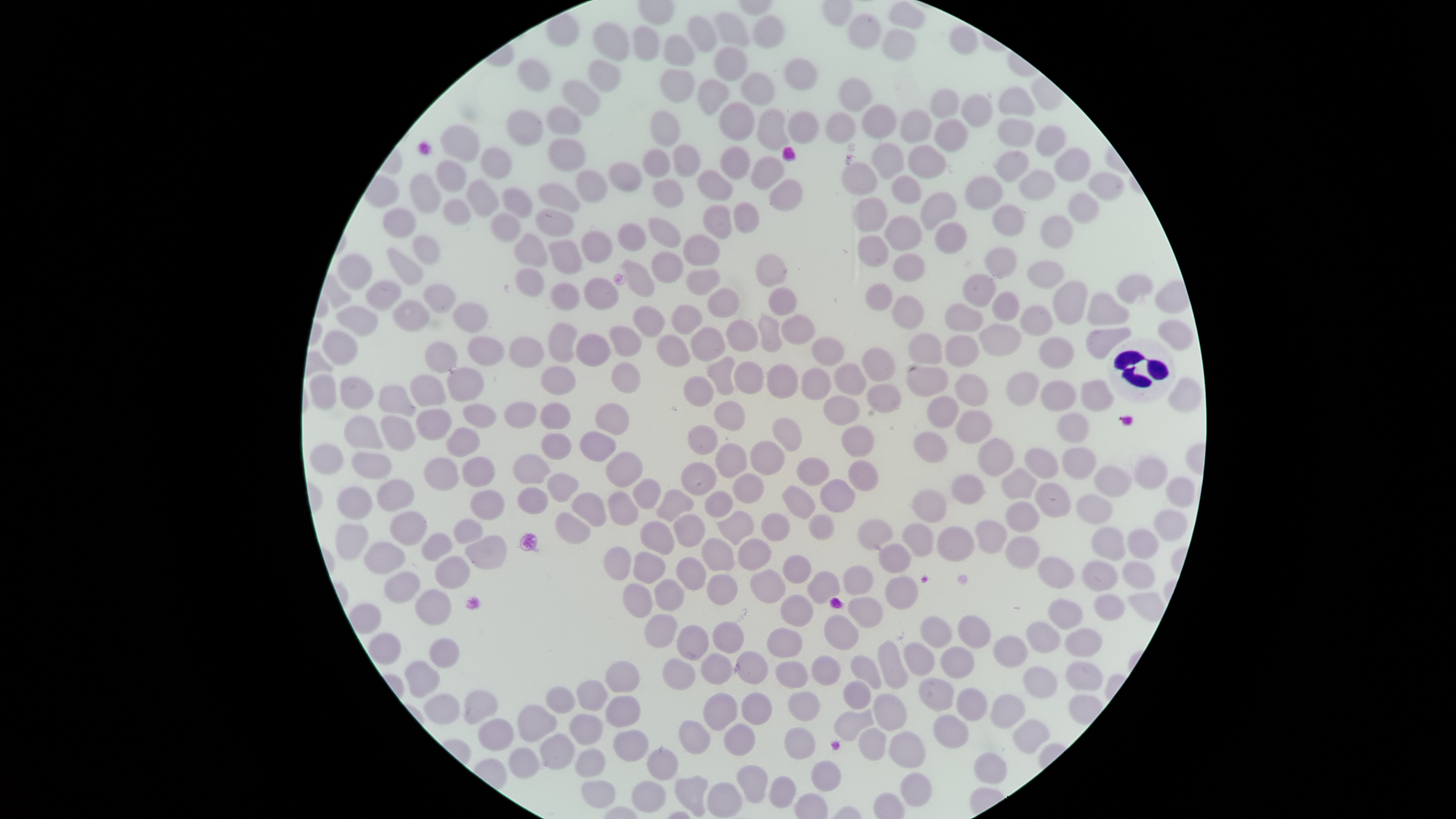

Approximate bounding boxes as (left, top, right, bottom) in pixels.
Summary:
  - Uninfected red blood cells: (889, 1, 925, 31), (714, 12, 751, 48), (753, 14, 784, 49), (848, 14, 881, 52), (688, 17, 717, 53), (592, 22, 631, 61), (634, 26, 659, 61), (949, 27, 978, 55), (883, 29, 915, 62), (664, 35, 695, 68), (714, 48, 748, 81), (785, 58, 817, 89), (519, 59, 552, 92), (588, 60, 622, 91), (662, 69, 695, 103), (740, 72, 775, 106), (697, 78, 729, 115), (838, 79, 872, 112), (562, 81, 601, 116), (999, 86, 1036, 118), (931, 89, 959, 118), (961, 95, 991, 127), (719, 102, 754, 140), (861, 105, 896, 138), (547, 107, 583, 136), (756, 108, 789, 152), (507, 110, 543, 146), (651, 110, 680, 147), (900, 110, 931, 143), (788, 111, 818, 144), (825, 113, 855, 143), (998, 119, 1035, 147), (933, 120, 968, 152), (441, 125, 479, 163), (1035, 125, 1066, 158), (549, 138, 586, 171), (872, 143, 904, 179), (907, 144, 946, 179), (673, 145, 701, 177), (719, 146, 750, 179), (480, 147, 512, 179), (642, 147, 670, 179), (1055, 147, 1092, 182), (995, 150, 1029, 182), (751, 156, 784, 191), (436, 159, 467, 191), (608, 160, 642, 193), (842, 163, 878, 195), (576, 169, 608, 203), (697, 170, 732, 201), (1018, 170, 1057, 201), (1088, 171, 1125, 200), (409, 174, 441, 214), (892, 176, 920, 205), (965, 177, 1002, 210), (653, 178, 684, 208), (770, 178, 802, 211), (466, 179, 500, 218), (537, 182, 581, 215), (921, 192, 956, 230), (1068, 193, 1099, 223), (852, 198, 888, 233), (444, 199, 471, 225), (734, 201, 760, 233), (991, 205, 1025, 236), (703, 206, 731, 239), (535, 207, 574, 239), (383, 208, 416, 237), (649, 216, 681, 247), (882, 216, 922, 251), (1041, 216, 1073, 250), (934, 222, 968, 253), (617, 223, 646, 251), (581, 230, 612, 262), (515, 233, 548, 267), (684, 234, 719, 267), (412, 235, 441, 265), (856, 236, 888, 267), (549, 240, 583, 274), (985, 247, 1016, 278), (387, 248, 424, 285), (652, 251, 682, 284), (337, 254, 371, 290), (756, 254, 788, 287), (892, 254, 925, 281), (620, 259, 655, 297), (1028, 262, 1064, 287), (515, 268, 544, 297), (686, 268, 721, 295), (962, 272, 996, 307), (1117, 273, 1153, 303), (584, 278, 618, 309), (366, 281, 402, 311), (549, 281, 579, 311), (1054, 281, 1088, 324), (864, 283, 892, 310), (425, 284, 455, 313), (768, 287, 796, 315), (708, 288, 740, 319), (993, 293, 1020, 321), (1088, 293, 1130, 326), (892, 296, 924, 329), (393, 300, 429, 332), (452, 303, 486, 333), (944, 303, 983, 332), (672, 304, 703, 334), (337, 305, 378, 337), (632, 305, 665, 338), (1020, 305, 1053, 336), (757, 314, 782, 353), (781, 314, 815, 345), (1157, 320, 1193, 350), (547, 321, 577, 364), (726, 321, 758, 351), (979, 324, 1021, 356), (609, 326, 642, 357), (691, 327, 725, 361), (1085, 328, 1133, 359), (321, 331, 359, 367), (576, 333, 612, 367), (907, 334, 943, 363), (656, 335, 691, 367), (943, 336, 979, 366), (467, 337, 504, 366), (509, 337, 544, 368), (810, 337, 843, 365), (1040, 338, 1074, 368), (425, 342, 457, 374), (861, 348, 895, 382), (708, 355, 737, 396), (733, 361, 764, 394), (611, 363, 641, 393), (766, 363, 799, 399), (833, 363, 866, 396), (906, 365, 949, 398), (541, 366, 576, 396), (447, 367, 483, 401), (800, 369, 830, 400), (1007, 372, 1037, 407), (308, 373, 337, 409), (954, 373, 988, 406), (410, 375, 446, 407), (683, 376, 713, 406), (340, 377, 374, 408), (1169, 377, 1201, 413), (1082, 379, 1114, 412), (1041, 382, 1074, 411), (865, 383, 900, 411), (378, 386, 417, 418), (822, 393, 860, 426), (927, 396, 959, 428), (713, 400, 745, 430), (504, 402, 536, 428), (539, 402, 572, 431), (595, 403, 630, 436), (463, 404, 496, 429), (417, 409, 451, 439), (957, 410, 990, 445), (1059, 413, 1088, 444), (345, 415, 384, 449), (381, 416, 417, 450), (772, 419, 802, 451), (688, 424, 718, 456), (842, 424, 874, 458), (446, 429, 480, 456), (580, 431, 616, 462), (913, 432, 949, 462), (540, 433, 571, 460), (978, 438, 1014, 475), (751, 441, 786, 476), (715, 443, 747, 477), (309, 445, 344, 474), (1062, 448, 1096, 478), (1025, 449, 1058, 477), (352, 452, 391, 479), (606, 452, 643, 489), (512, 455, 550, 484), (1134, 455, 1169, 490), (462, 456, 494, 487), (798, 456, 829, 486), (423, 458, 459, 491), (848, 459, 879, 491), (681, 462, 716, 496), (1094, 466, 1131, 497), (1002, 467, 1036, 499), (547, 473, 579, 502), (734, 473, 766, 505), (953, 475, 984, 503), (634, 477, 662, 510), (1167, 477, 1196, 508), (819, 478, 855, 512), (377, 480, 415, 513), (781, 483, 816, 519), (1036, 483, 1070, 517), (337, 487, 371, 520), (518, 488, 548, 515), (657, 488, 695, 523), (469, 489, 505, 520), (912, 490, 946, 523), (704, 491, 732, 517), (571, 492, 608, 528), (608, 493, 639, 525), (1077, 494, 1112, 523), (1005, 501, 1038, 530), (1154, 510, 1186, 541), (716, 511, 755, 545), (389, 512, 426, 544), (555, 512, 591, 544), (761, 512, 790, 541), (675, 514, 706, 548), (809, 515, 833, 538), (858, 518, 894, 550), (453, 519, 484, 544), (975, 519, 1007, 554), (639, 523, 674, 555), (902, 523, 935, 557), (336, 524, 368, 560), (937, 526, 974, 562), (1092, 526, 1126, 560), (1128, 528, 1158, 560), (421, 533, 454, 562), (464, 535, 507, 569), (701, 538, 734, 572), (738, 538, 771, 570), (365, 541, 405, 574), (879, 544, 911, 573), (604, 547, 632, 580), (633, 551, 666, 583), (783, 556, 811, 583), (435, 557, 471, 588), (677, 557, 706, 590), (1037, 557, 1074, 590), (1082, 560, 1117, 591), (1123, 560, 1156, 590), (844, 566, 874, 596), (749, 569, 787, 604), (385, 571, 421, 604), (807, 572, 839, 604), (706, 575, 737, 605), (884, 577, 919, 609), (654, 579, 684, 610), (623, 584, 652, 617), (415, 588, 450, 625), (1094, 593, 1125, 622), (780, 594, 813, 628), (849, 597, 883, 628), (1048, 598, 1083, 629), (958, 614, 991, 648), (645, 615, 678, 647), (825, 616, 859, 650), (922, 617, 952, 648), (713, 622, 744, 654), (1026, 622, 1061, 654), (677, 625, 709, 660), (767, 627, 803, 658), (1063, 628, 1103, 658), (368, 633, 402, 664), (993, 635, 1027, 669), (429, 639, 460, 669), (878, 642, 908, 689), (903, 643, 934, 677), (941, 648, 974, 679), (737, 651, 768, 684), (701, 654, 733, 686), (812, 655, 842, 685), (850, 655, 882, 690), (663, 658, 696, 690), (404, 660, 439, 698), (605, 661, 639, 692), (776, 661, 809, 690), (1066, 661, 1103, 691), (1023, 666, 1059, 700), (919, 677, 954, 711), (576, 679, 608, 711), (844, 680, 872, 710), (547, 687, 575, 714), (956, 688, 987, 721), (464, 689, 497, 725), (703, 692, 738, 731), (740, 692, 771, 725), (787, 692, 821, 720), (424, 694, 459, 724), (874, 695, 906, 730), (991, 695, 1026, 729), (606, 696, 639, 728), (517, 705, 558, 743), (835, 710, 875, 741), (932, 714, 969, 748), (571, 715, 602, 746), (478, 719, 513, 750), (1011, 719, 1051, 755), (679, 721, 712, 754), (725, 723, 755, 755), (785, 728, 816, 759), (858, 728, 886, 761), (613, 730, 649, 760), (889, 732, 926, 767), (540, 734, 576, 769), (509, 748, 540, 778), (646, 748, 678, 781), (576, 750, 606, 777), (974, 752, 1007, 785), (810, 761, 841, 791), (737, 766, 768, 802), (900, 771, 932, 807), (674, 775, 707, 817), (769, 775, 797, 809), (581, 781, 616, 808), (631, 781, 666, 812), (707, 781, 742, 818)
  - White blood cells: (1106, 337, 1176, 403)
  - Stain: Giemsa
  - Preparation: thin blood film
  - Visible region: circular
  - Field of view: single
  - Image size: 1456×819 pixels
  - Presence: no malaria parasites detected
  - Capture: smartphone photograph through the microscope eyepiece